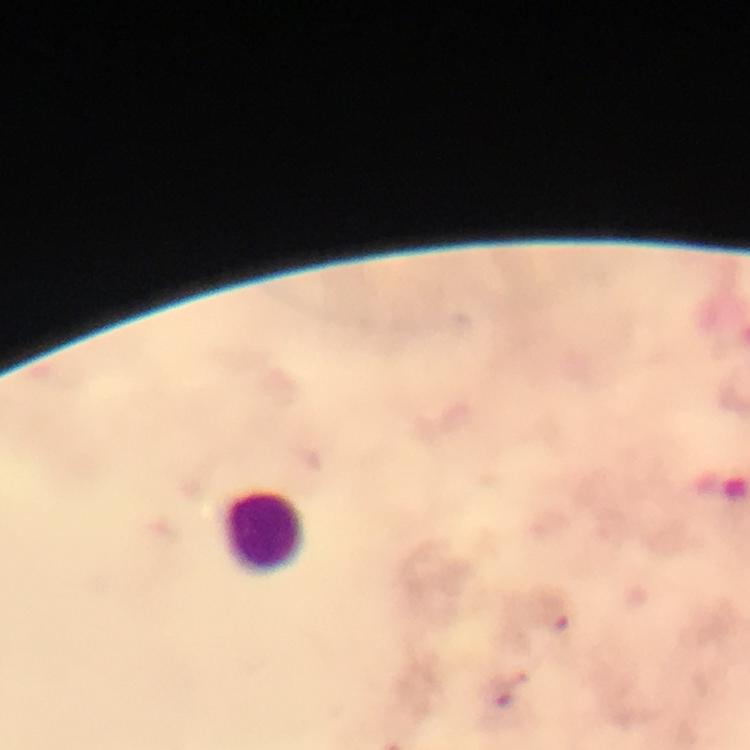 Approximate centers as [x, y] in pixels. Leukocyte locations: [265, 532]. Plasmodium parasite locations: [557, 615], [499, 695]. Giemsa-stained preparation. From a diagnostic examination for malaria. Photographed with a smartphone mounted on the microscope. Thick smear. 100x magnification. Immersion oil applied. Cropped region of a single field of view. Image is 750×750 pixels.